Name the cell type shown.
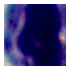

This is a leukocyte.

Summary:
  - Modality: photomicrograph
  - Magnification: 1000x